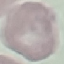

Summary:
  - Result: no malaria parasites detected
  - Stain: Giemsa
  - Preparation: thin smear
  - Image type: cell patch, automatically extracted from a larger field of view and resized to 64 × 64 pixels
  - Capture: smartphone camera at the microscope eyepiece